Report the malaria status of this cell.
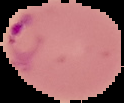
It is parasitized.

{
  "image_type": "cell region segmented out of the field of view; surrounding area masked to black",
  "image_size": "124×103 pixels",
  "preparation": "thin blood film"
}